Classify this cell by malaria status.
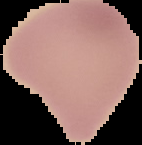
It is uninfected.

From a thin blood film. Cell region segmented out of the field of view; the surrounding area is masked to black. Image is 142×145 pixels.